Locate every Plasmodium parasite and every leukocyte.
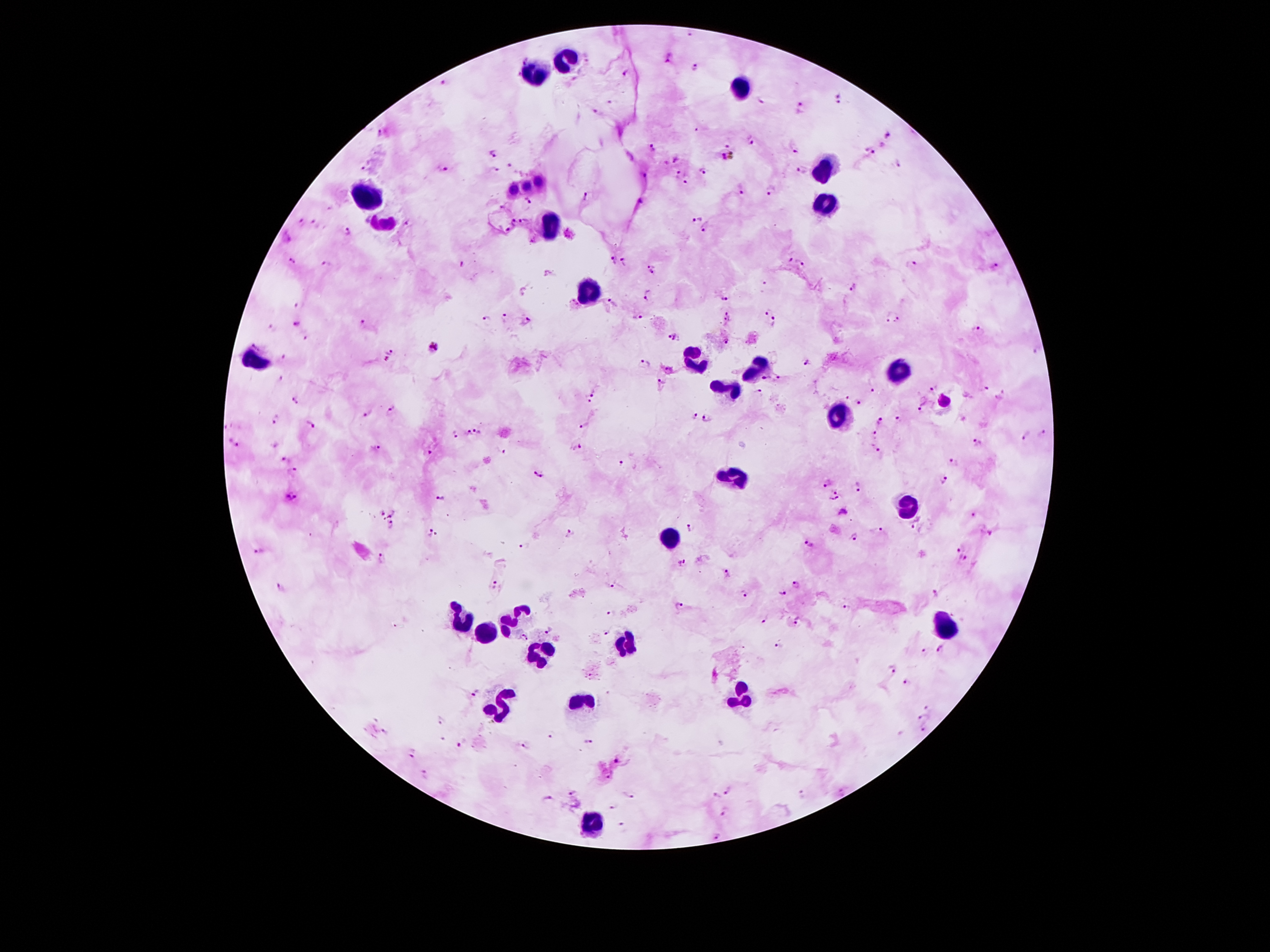

Approximate centers as (x, y) in pixels.
Plasmodium parasites: (688, 33), (670, 59), (696, 67), (627, 73), (444, 84), (838, 98), (761, 101), (610, 103), (804, 107), (597, 112), (380, 133), (890, 136), (751, 141), (652, 147), (795, 148), (870, 150), (493, 155), (726, 156), (677, 157), (897, 163), (510, 165), (443, 167), (362, 168), (497, 170), (801, 170), (704, 171), (645, 175), (676, 177), (538, 180), (687, 182), (525, 186), (512, 188), (740, 188), (770, 192), (588, 195), (530, 201), (642, 201), (698, 217), (513, 222), (524, 222), (407, 223), (303, 224), (316, 224), (706, 228), (346, 231), (507, 231), (614, 259), (791, 259), (293, 262), (626, 262), (461, 264), (803, 264), (911, 264), (995, 264), (327, 265), (653, 272), (854, 288), (649, 296), (725, 298), (614, 303), (298, 306), (767, 310), (505, 317), (640, 317), (897, 319), (484, 320), (887, 320), (527, 322), (364, 323), (774, 323), (296, 324), (269, 327), (976, 329), (676, 336), (304, 338), (727, 342), (434, 350), (1038, 350), (391, 351), (283, 355), (386, 361), (809, 362), (645, 363), (667, 368), (280, 378), (765, 378), (779, 378), (661, 383), (931, 388), (985, 388), (758, 390), (874, 390), (591, 395), (297, 398), (847, 398), (996, 398), (860, 402), (945, 402), (920, 408), (392, 410), (367, 413), (694, 414), (707, 417), (880, 420), (898, 420), (275, 421), (308, 423), (583, 426), (479, 429), (467, 432), (454, 433), (1042, 433), (873, 434), (1024, 436), (234, 442), (976, 443), (576, 447), (376, 449), (874, 449), (504, 452), (430, 453), (285, 458), (954, 461), (621, 463), (293, 470), (537, 475), (944, 481), (826, 483), (858, 487), (836, 490), (292, 497), (441, 497), (833, 499), (382, 513), (392, 514), (974, 516), (389, 526), (915, 526), (690, 529), (426, 531), (879, 531), (987, 532), (569, 534), (853, 536), (809, 544), (960, 546), (526, 548), (259, 550), (383, 558), (964, 558), (683, 561), (725, 573), (494, 585), (610, 585), (281, 586), (795, 586), (782, 592), (934, 592), (743, 593), (679, 606), (845, 607), (611, 613), (764, 619), (796, 621), (550, 629), (609, 632), (523, 638), (779, 647), (941, 648), (922, 651), (893, 669), (906, 682), (475, 692), (927, 708), (921, 716), (440, 721), (924, 730), (550, 735), (461, 742), (588, 742), (523, 747), (411, 752), (617, 759), (425, 774), (608, 776), (571, 791), (727, 791), (802, 794), (630, 795), (714, 795), (612, 808), (724, 812), (622, 824), (716, 834).
Leukocytes: (569, 58), (535, 72), (740, 89), (824, 170), (364, 197), (830, 203), (553, 226), (591, 291), (696, 356), (255, 363), (895, 371), (756, 372), (727, 388), (840, 415), (735, 474), (909, 508), (672, 540), (458, 620), (516, 620), (943, 630), (486, 634), (623, 646), (541, 654), (738, 693), (581, 705), (501, 707), (594, 823).

Summary:
  - Stain: Giemsa
  - Patient malaria status: infected with Plasmodium falciparum
  - Preparation: thick blood smear
  - Field of view: single
  - Magnification: 100x
  - Image size: 1270×952 pixels
  - Capture: smartphone camera through the microscope eyepiece